Assess this cell for malaria.
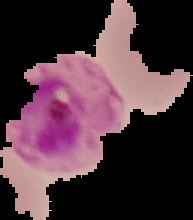
It is parasitized.

From a thin blood film. Image is 193×220 pixels. Cell region segmented out of the field of view; the surrounding area is masked to black.